Report the malaria status of this cell.
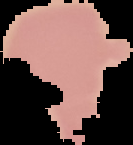
Uninfected.

image type = segmented cell region on a black background
image size = 133×145 pixels
preparation = thin blood smear